State which parasite is depicted.
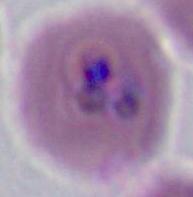
This is Plasmodium.

magnification = 400x or 1000x
modality = micrograph